Identify the parasite.
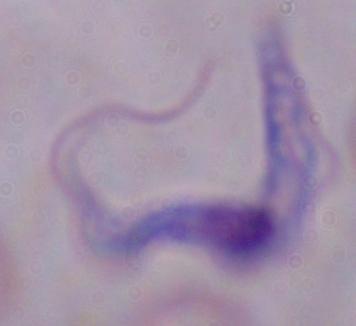
This is a trypanosome.

magnification = 1000x
modality = micrograph